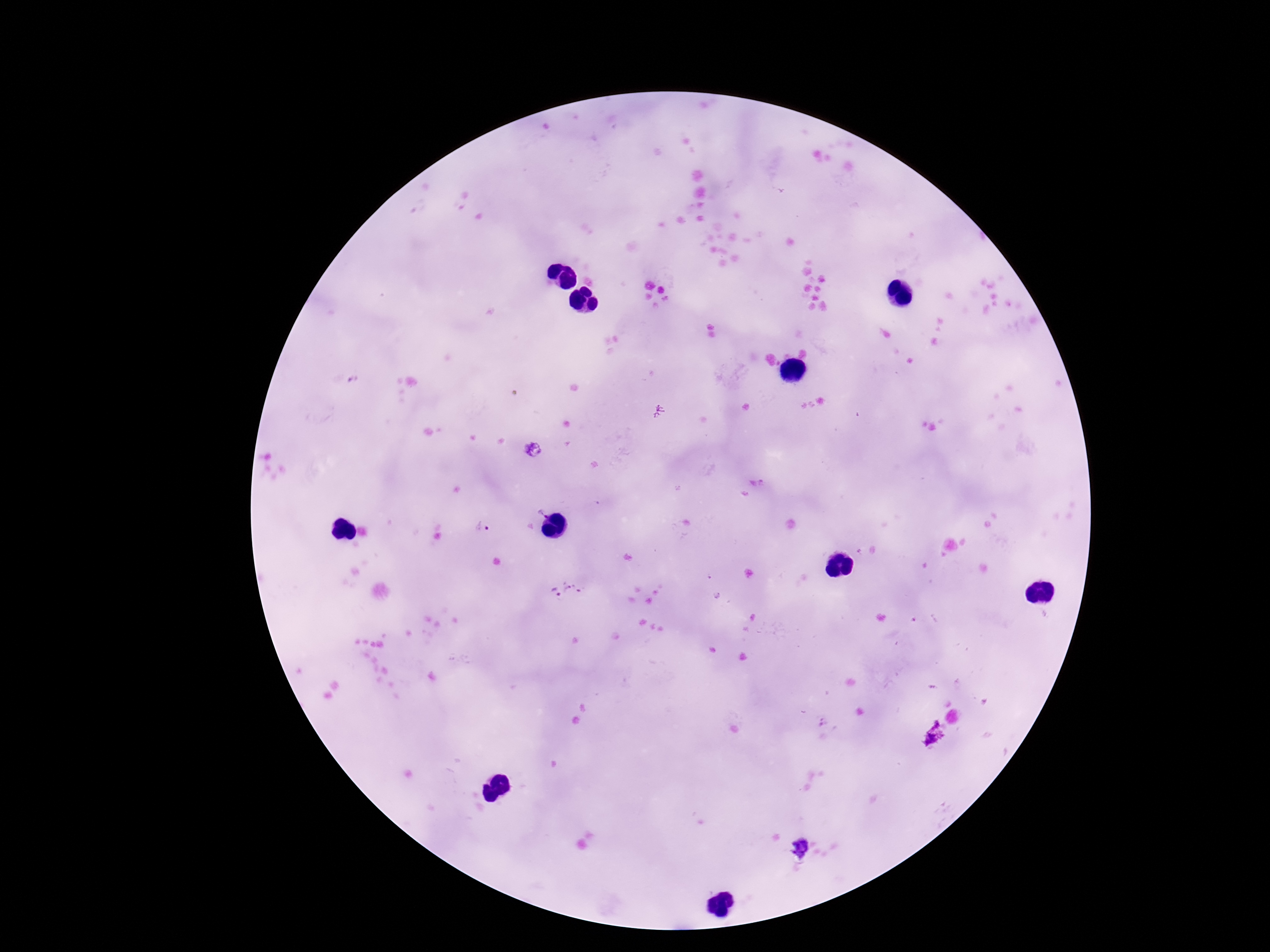
Approximate centers as [x, y] in pixels.
Summary:
  - Plasmodium parasite locations: [353, 379], [658, 411], [531, 449], [757, 480], [541, 512], [481, 527], [567, 592], [802, 847]
  - Capture: smartphone camera through the microscope eyepiece
  - Magnification: 100x
  - Field of view: single
  - Preparation: thick peripheral-blood smear
  - Image size: 1270×952 pixels
  - Stain: Giemsa
  - Patient malaria status: positive